Locate every Plasmodium falciparum-infected red blood cell.
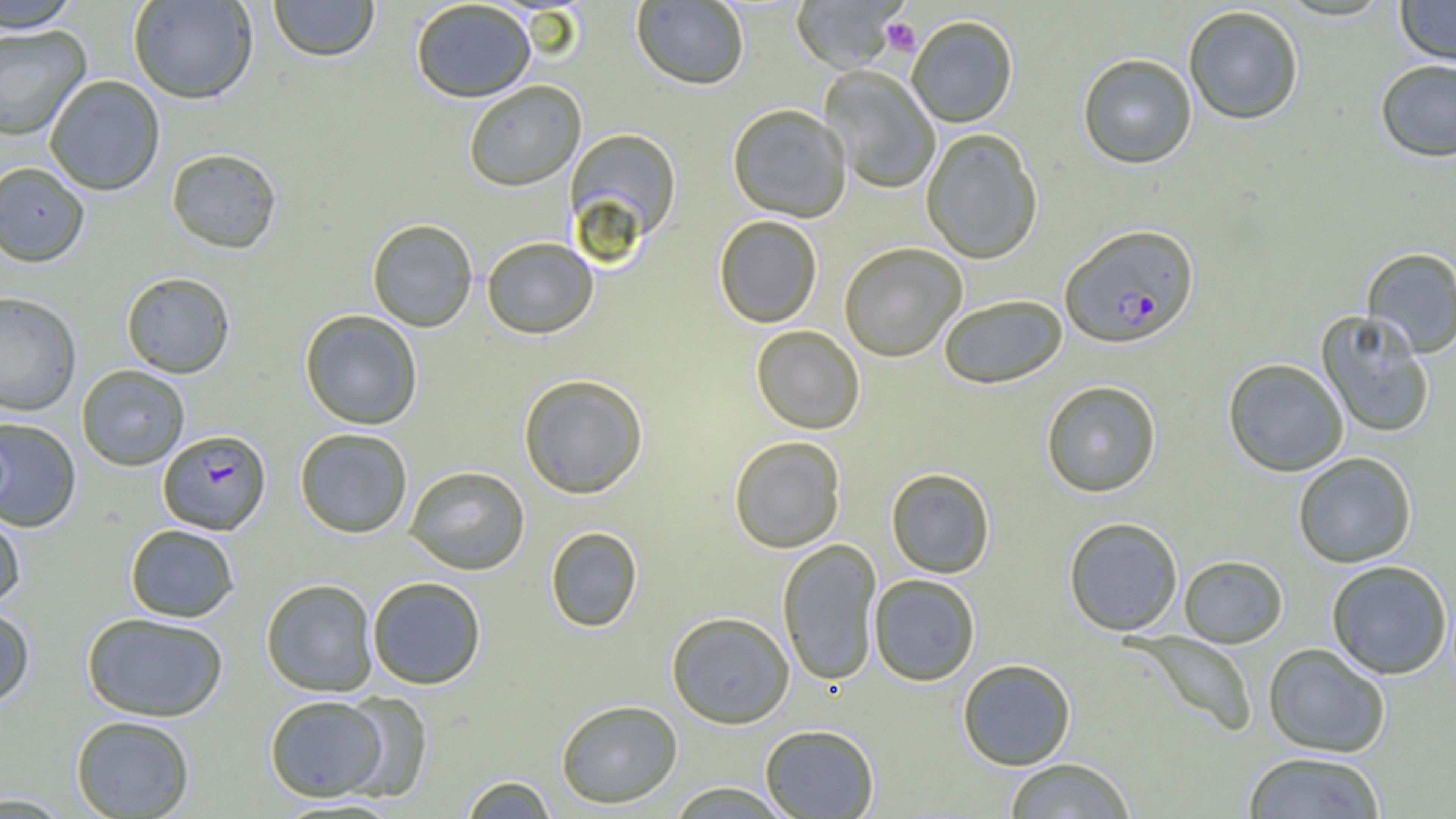
Approximate bounding boxes as (x1, y1, x2, y2) in pixels.
Plasmodium falciparum-infected red blood cells: (1060, 224, 1200, 349), (158, 429, 272, 534).

Platelet locations: (880, 17, 921, 57). Uninfected red blood cell locations: (1, 0, 81, 33), (127, 0, 259, 104), (268, 0, 380, 62), (790, 0, 909, 74), (1395, 0, 1456, 67), (410, 1, 536, 103), (631, 1, 749, 90), (1182, 5, 1305, 126), (906, 15, 1018, 128), (0, 25, 92, 141), (1078, 53, 1197, 169), (1374, 59, 1456, 162), (819, 66, 941, 194), (44, 75, 165, 196), (463, 81, 586, 191), (727, 103, 852, 222), (565, 127, 682, 246), (921, 128, 1043, 264), (166, 147, 283, 254), (0, 162, 90, 267), (714, 215, 823, 328), (366, 218, 477, 332), (481, 235, 599, 339), (839, 242, 967, 362), (1360, 247, 1456, 358), (120, 271, 236, 378), (0, 291, 81, 416), (938, 293, 1068, 389), (299, 309, 423, 430), (1316, 310, 1436, 439), (751, 325, 865, 434), (1222, 358, 1349, 477), (76, 365, 190, 471), (518, 373, 648, 499), (1041, 380, 1162, 498), (0, 417, 82, 532), (294, 427, 413, 538), (728, 436, 846, 553), (1292, 451, 1417, 568), (403, 465, 530, 575), (886, 467, 995, 578), (0, 509, 27, 610), (1063, 516, 1183, 636), (125, 524, 240, 622), (545, 526, 643, 632), (777, 539, 882, 686), (1179, 555, 1289, 648), (1325, 560, 1454, 680), (868, 574, 981, 686), (367, 576, 487, 689), (261, 578, 379, 697), (0, 605, 36, 709), (666, 611, 795, 729), (81, 612, 229, 722), (1123, 631, 1259, 738), (1262, 642, 1391, 757), (957, 658, 1076, 770), (338, 691, 433, 803), (264, 694, 390, 801), (555, 699, 683, 808), (70, 715, 195, 818), (760, 724, 880, 818), (1242, 751, 1386, 818), (1003, 757, 1136, 818), (459, 775, 558, 819), (665, 781, 793, 818), (0, 792, 74, 817). Slide-level diagnosis: Plasmodium falciparum. Single field of view. Image is 1456×819 pixels. 1000x magnification. Thin blood film. Light microscopy.